Look for Plasmodium parasites.
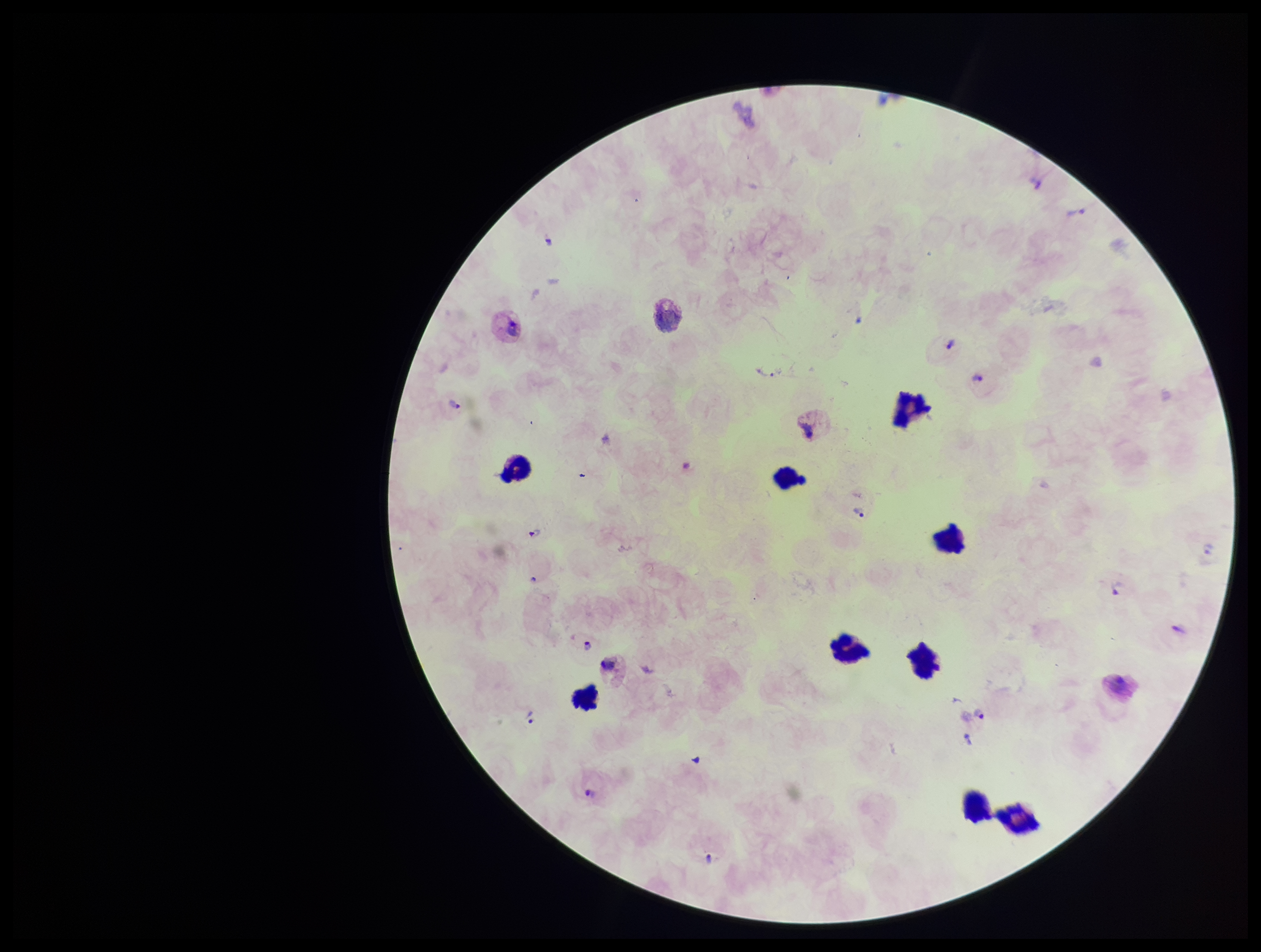

Seen.

Summary:
  - Preparation: thick smear
  - Capture: smartphone photograph through the microscope eyepiece
  - Patient malaria status: infected
  - Parasite count: 9
  - Species reported for this patient: Plasmodium vivax
  - Image size: 1261×952 pixels
  - Stain: Giemsa
  - Leukocyte count: 9
  - Field of view: single